Report the malaria status of this cell.
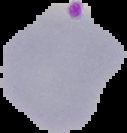

Parasitized.

{
  "image_type": "segmented cell region on a black background",
  "image_size": "127×133 pixels",
  "preparation": "thin blood smear"
}